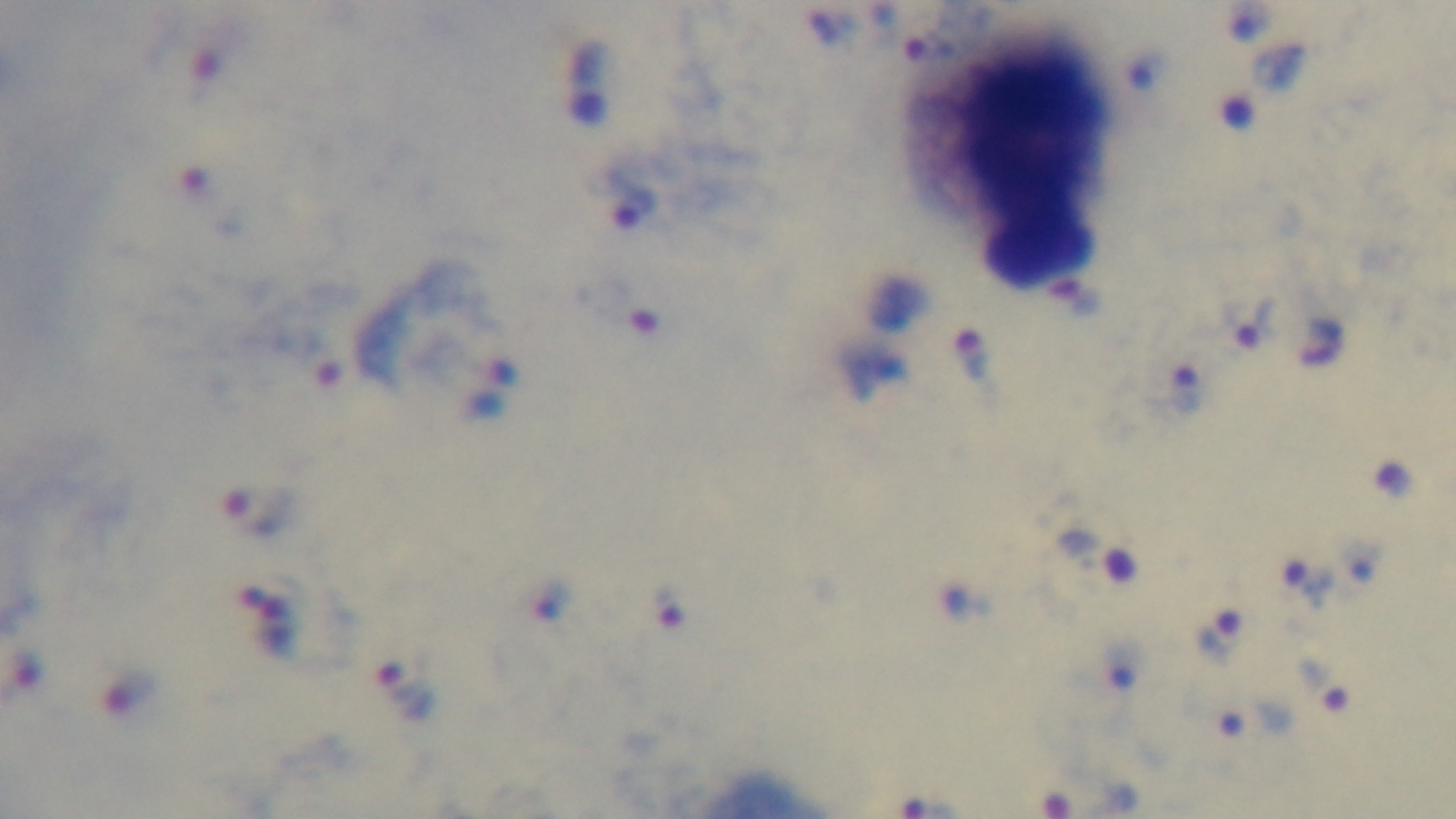
{
  "modality": "light microscopy",
  "malaria_status": "infected",
  "field_of_view": "single",
  "preparation": "thick smear",
  "objective": "100x oil immersion",
  "stain": "Giemsa",
  "capture": "mounted 4K digital camera"
}